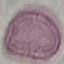 Malaria status: uninfected. Giemsa-stained preparation. Thin blood film. Acquired by smartphone through the microscope eyepiece. Automatically extracted cell patch, resized to 64 × 64 pixels.